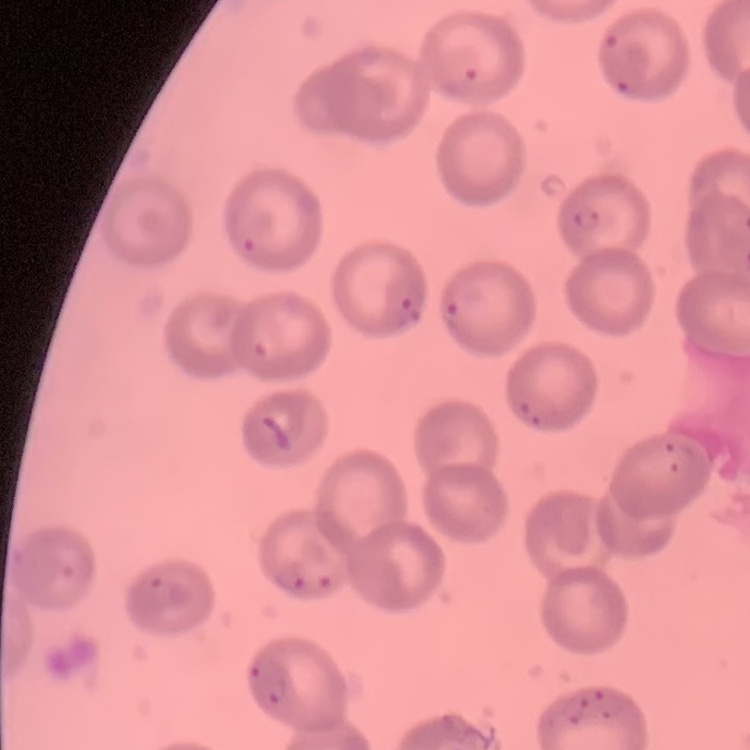
red blood cell morphology = no rouleaux formation
stain = Field's or Giemsa
preparation = thin blood film
image type = square crop of a larger photomicrograph